Name the blood parasite species.
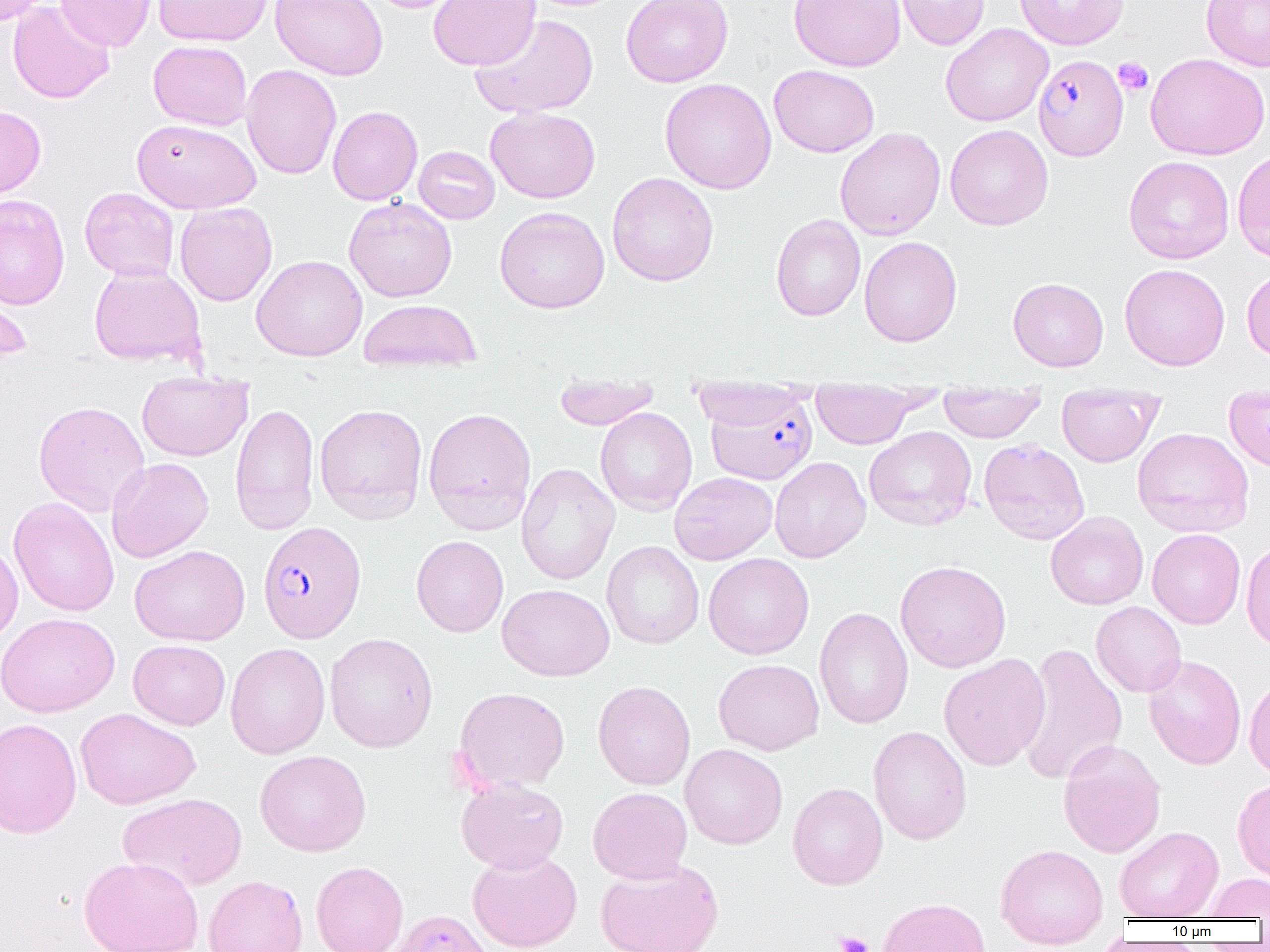

Plasmodium falciparum.

Summary:
  - Coordinate format: approximate bounding boxes as [x1, y1, x2, y2] in pixels
  - Uninfected red blood cell locations: [0, 0, 50, 25], [56, 0, 157, 51], [152, 0, 273, 47], [270, 0, 389, 80], [360, 0, 468, 13], [428, 0, 540, 70], [621, 0, 734, 87], [788, 0, 905, 71], [895, 0, 990, 50], [1015, 0, 1129, 50], [1200, 0, 1270, 71], [8, 1, 114, 104], [470, 13, 599, 119], [940, 23, 1053, 126], [148, 40, 252, 130], [1145, 53, 1269, 160], [769, 64, 880, 157], [241, 65, 342, 179], [659, 78, 777, 194], [0, 105, 46, 202], [327, 105, 423, 205], [486, 106, 600, 203], [132, 119, 261, 213], [945, 124, 1053, 230], [835, 127, 946, 240], [413, 146, 500, 224], [1232, 147, 1270, 264], [1123, 155, 1235, 264], [607, 172, 719, 286], [80, 187, 179, 282], [0, 194, 70, 310], [344, 197, 457, 302], [175, 202, 277, 306], [495, 206, 609, 314], [770, 213, 866, 321], [859, 236, 962, 347], [251, 254, 367, 361], [1119, 263, 1230, 370], [88, 264, 206, 367], [1242, 266, 1270, 363], [1008, 277, 1109, 371], [0, 282, 32, 366], [359, 298, 481, 374], [136, 371, 252, 461], [552, 379, 662, 429], [688, 386, 816, 429], [811, 388, 920, 449], [938, 390, 1046, 442], [1056, 395, 1161, 466], [1223, 395, 1270, 473], [33, 401, 150, 516], [230, 402, 320, 535], [314, 403, 428, 525], [423, 406, 537, 534], [594, 407, 697, 515], [864, 426, 977, 531], [1132, 427, 1254, 538], [979, 438, 1090, 545], [769, 456, 871, 563], [106, 457, 213, 563], [516, 463, 619, 585], [669, 472, 778, 565], [8, 497, 120, 617], [1045, 511, 1148, 610], [1148, 528, 1246, 629], [411, 535, 508, 637], [0, 538, 22, 649], [602, 541, 704, 649], [1241, 542, 1270, 652], [129, 544, 250, 646], [703, 553, 814, 659], [895, 560, 1011, 673], [497, 584, 614, 681], [1091, 602, 1186, 697], [814, 607, 914, 730], [0, 612, 120, 717], [324, 633, 438, 752], [128, 639, 230, 730], [1016, 642, 1127, 786], [225, 643, 330, 759], [939, 654, 1050, 771], [1143, 655, 1246, 770], [713, 658, 824, 755], [1244, 674, 1270, 781], [592, 680, 695, 790], [453, 687, 570, 793], [76, 708, 200, 809], [0, 718, 82, 839], [868, 726, 972, 845], [1058, 741, 1166, 858], [680, 744, 788, 849], [255, 750, 371, 856], [456, 777, 569, 874], [1232, 778, 1270, 883], [787, 783, 888, 890], [588, 787, 692, 884], [118, 792, 248, 891], [1115, 826, 1224, 920], [995, 844, 1109, 950], [467, 849, 582, 952], [79, 856, 204, 952], [594, 859, 725, 952], [311, 861, 408, 952], [1204, 873, 1270, 919], [203, 875, 308, 952], [876, 897, 991, 952]
  - Platelet locations: [1114, 58, 1153, 96], [833, 931, 873, 952]
  - Plasmodium falciparum-infected red blood cell locations: [1033, 54, 1128, 161], [703, 393, 818, 485], [257, 520, 366, 644], [388, 909, 495, 952]
  - Magnification: 1000x
  - Modality: optical microscopy
  - Preparation: thin blood smear
  - Image size: 1270×952 pixels
  - Field of view: one of a larger specimen